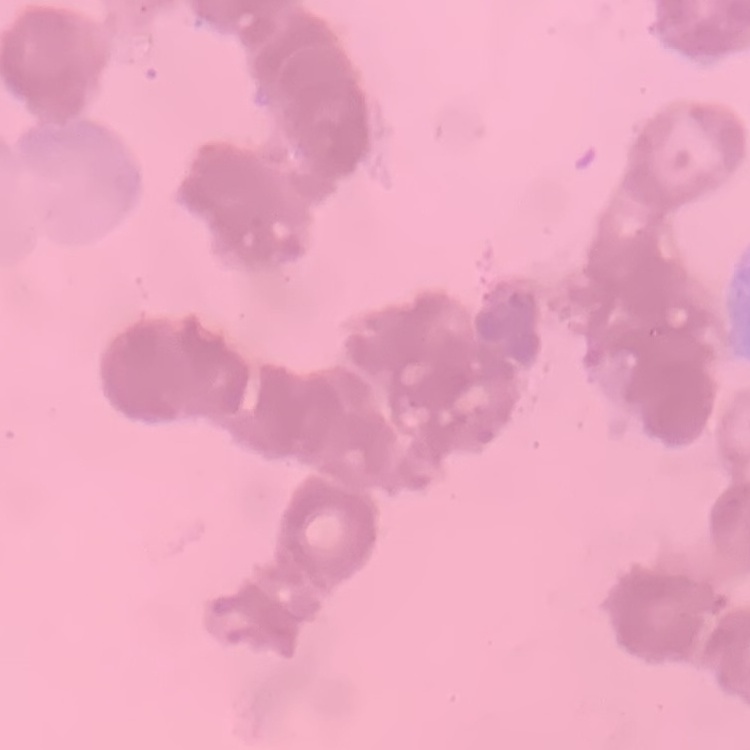

The erythrocytes show rouleaux formation. Thin blood smear. Field's or Giemsa stain. One tile cut from a larger photomicrograph.